Identify the parasite.
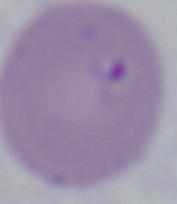

Babesia.

Summary:
  - Magnification: 1000x
  - Modality: photomicrograph